Locate and identify every blood parasite.
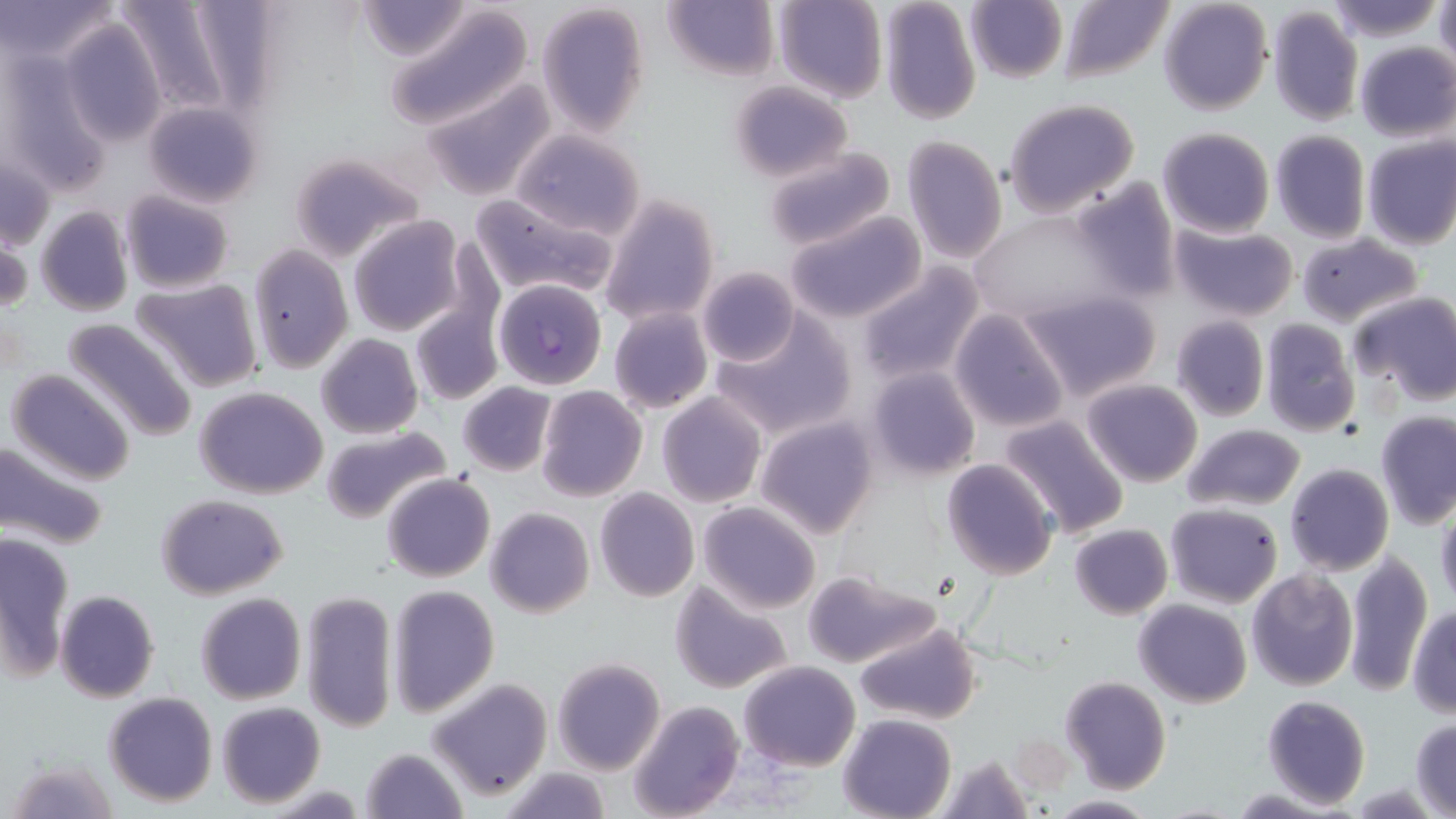
Approximate bounding boxes as named x1/y1/x2/y2 corners in pixels.
Plasmodium falciparum-infected red blood cells: (x1=494, y1=279, x2=605, y2=389).
No Plasmodium ovale, Plasmodium malariae, Plasmodium vivax, Babesia divergens, or Trypanosoma brucei observed.

Summary:
  - Uninfected red blood cell locations: (x1=0, y1=0, x2=121, y2=69), (x1=111, y1=0, x2=250, y2=119), (x1=356, y1=0, x2=473, y2=62), (x1=773, y1=0, x2=887, y2=103), (x1=1060, y1=0, x2=1174, y2=84), (x1=1158, y1=0, x2=1272, y2=115), (x1=1324, y1=0, x2=1442, y2=41), (x1=663, y1=1, x2=778, y2=82), (x1=877, y1=1, x2=982, y2=126), (x1=964, y1=1, x2=1066, y2=84), (x1=1434, y1=1, x2=1456, y2=68), (x1=538, y1=3, x2=650, y2=136), (x1=384, y1=4, x2=533, y2=130), (x1=1266, y1=7, x2=1363, y2=128), (x1=61, y1=18, x2=168, y2=147), (x1=1354, y1=41, x2=1456, y2=144), (x1=0, y1=45, x2=110, y2=194), (x1=422, y1=78, x2=555, y2=202), (x1=726, y1=81, x2=853, y2=182), (x1=1004, y1=98, x2=1139, y2=216), (x1=143, y1=101, x2=263, y2=208), (x1=1157, y1=126, x2=1274, y2=239), (x1=508, y1=127, x2=648, y2=240), (x1=1269, y1=130, x2=1370, y2=243), (x1=902, y1=136, x2=1006, y2=264), (x1=1361, y1=136, x2=1456, y2=251), (x1=760, y1=146, x2=898, y2=254), (x1=285, y1=151, x2=422, y2=263), (x1=1, y1=152, x2=55, y2=254), (x1=313, y1=165, x2=448, y2=309), (x1=1065, y1=179, x2=1179, y2=304), (x1=119, y1=190, x2=234, y2=294), (x1=470, y1=194, x2=619, y2=301), (x1=599, y1=194, x2=721, y2=329), (x1=36, y1=207, x2=133, y2=317), (x1=968, y1=210, x2=1121, y2=330), (x1=785, y1=212, x2=926, y2=323), (x1=347, y1=215, x2=466, y2=337), (x1=1169, y1=222, x2=1299, y2=321), (x1=1, y1=226, x2=30, y2=319), (x1=1295, y1=233, x2=1421, y2=327), (x1=248, y1=246, x2=351, y2=373), (x1=856, y1=263, x2=985, y2=385), (x1=697, y1=266, x2=800, y2=367), (x1=131, y1=276, x2=264, y2=393), (x1=1020, y1=290, x2=1162, y2=402), (x1=1351, y1=291, x2=1456, y2=404), (x1=410, y1=303, x2=502, y2=404), (x1=608, y1=307, x2=711, y2=414), (x1=948, y1=309, x2=1071, y2=433), (x1=714, y1=310, x2=857, y2=440), (x1=1170, y1=315, x2=1269, y2=423), (x1=62, y1=317, x2=199, y2=441), (x1=1259, y1=319, x2=1361, y2=437), (x1=316, y1=333, x2=422, y2=440), (x1=864, y1=365, x2=981, y2=483), (x1=5, y1=369, x2=137, y2=487), (x1=1081, y1=378, x2=1202, y2=487), (x1=457, y1=382, x2=556, y2=477), (x1=536, y1=384, x2=648, y2=501), (x1=195, y1=386, x2=329, y2=497), (x1=657, y1=392, x2=767, y2=507), (x1=1375, y1=411, x2=1456, y2=529), (x1=997, y1=413, x2=1132, y2=539), (x1=754, y1=415, x2=879, y2=538), (x1=1182, y1=424, x2=1306, y2=512), (x1=320, y1=425, x2=452, y2=526), (x1=0, y1=438, x2=111, y2=551), (x1=941, y1=458, x2=1058, y2=580), (x1=1284, y1=464, x2=1394, y2=576), (x1=382, y1=472, x2=495, y2=583), (x1=593, y1=487, x2=699, y2=601), (x1=156, y1=493, x2=288, y2=600), (x1=697, y1=502, x2=821, y2=614), (x1=1163, y1=502, x2=1282, y2=608), (x1=485, y1=507, x2=595, y2=617), (x1=1435, y1=508, x2=1456, y2=614), (x1=1069, y1=523, x2=1172, y2=619), (x1=2, y1=532, x2=74, y2=677), (x1=1344, y1=548, x2=1434, y2=696), (x1=802, y1=569, x2=941, y2=669), (x1=1246, y1=570, x2=1359, y2=692), (x1=670, y1=581, x2=794, y2=694), (x1=387, y1=584, x2=499, y2=717), (x1=54, y1=589, x2=160, y2=703), (x1=302, y1=589, x2=397, y2=734), (x1=196, y1=592, x2=306, y2=705), (x1=1135, y1=598, x2=1252, y2=707), (x1=1408, y1=607, x2=1456, y2=718), (x1=854, y1=620, x2=979, y2=727), (x1=552, y1=657, x2=664, y2=774), (x1=738, y1=660, x2=860, y2=770), (x1=1060, y1=675, x2=1171, y2=793), (x1=427, y1=679, x2=551, y2=801), (x1=103, y1=691, x2=217, y2=807), (x1=1262, y1=694, x2=1369, y2=810), (x1=216, y1=701, x2=326, y2=808), (x1=630, y1=701, x2=744, y2=819), (x1=837, y1=713, x2=957, y2=819), (x1=1410, y1=718, x2=1455, y2=817), (x1=358, y1=747, x2=469, y2=819), (x1=934, y1=753, x2=1035, y2=819), (x1=5, y1=757, x2=119, y2=816), (x1=493, y1=766, x2=619, y2=819), (x1=1048, y1=794, x2=1156, y2=817)
  - Slide-level diagnosis: Plasmodium falciparum
  - Stain: May-Grünwald-Giemsa
  - Magnification: 1000x
  - Modality: light microscopy
  - Image size: 1456×819 pixels
  - Field of view: single
  - Preparation: thin blood film